Describe the morphology of the red blood cells.
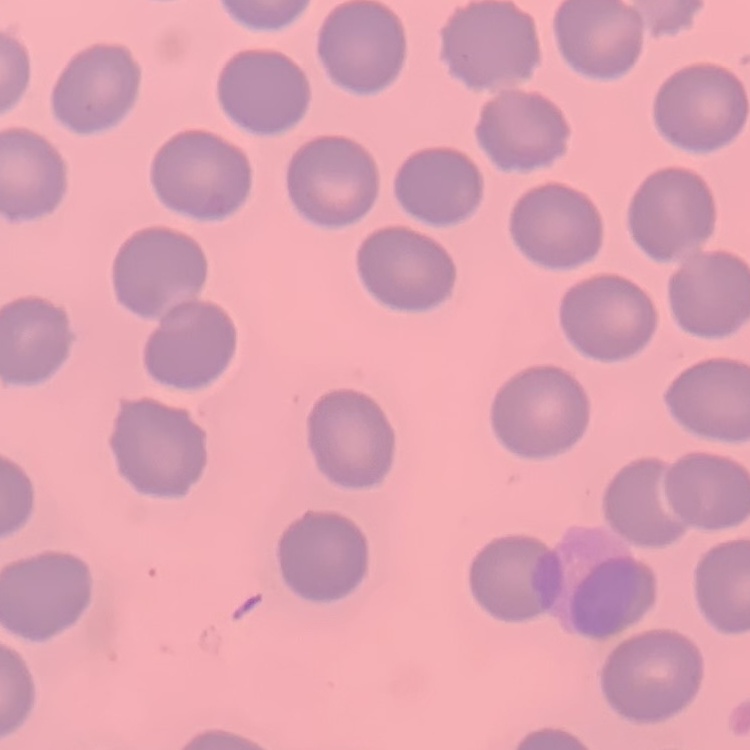

They show no rouleaux formation.

Summary:
  - Preparation: thin peripheral smear
  - Image type: one tile cut from a larger photomicrograph
  - Stain: Field's or Giemsa